Comment on the morphology of the erythrocytes.
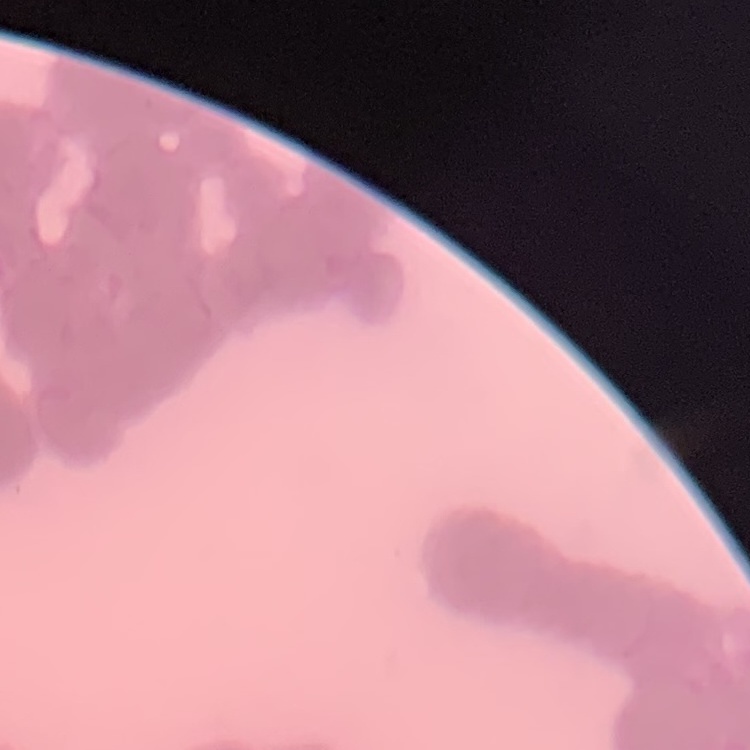
They show rouleaux formation.

Summary:
  - Preparation: thin blood smear
  - Stain: Field's or Giemsa
  - Image type: one tile cut from a larger photomicrograph